State the preparation type.
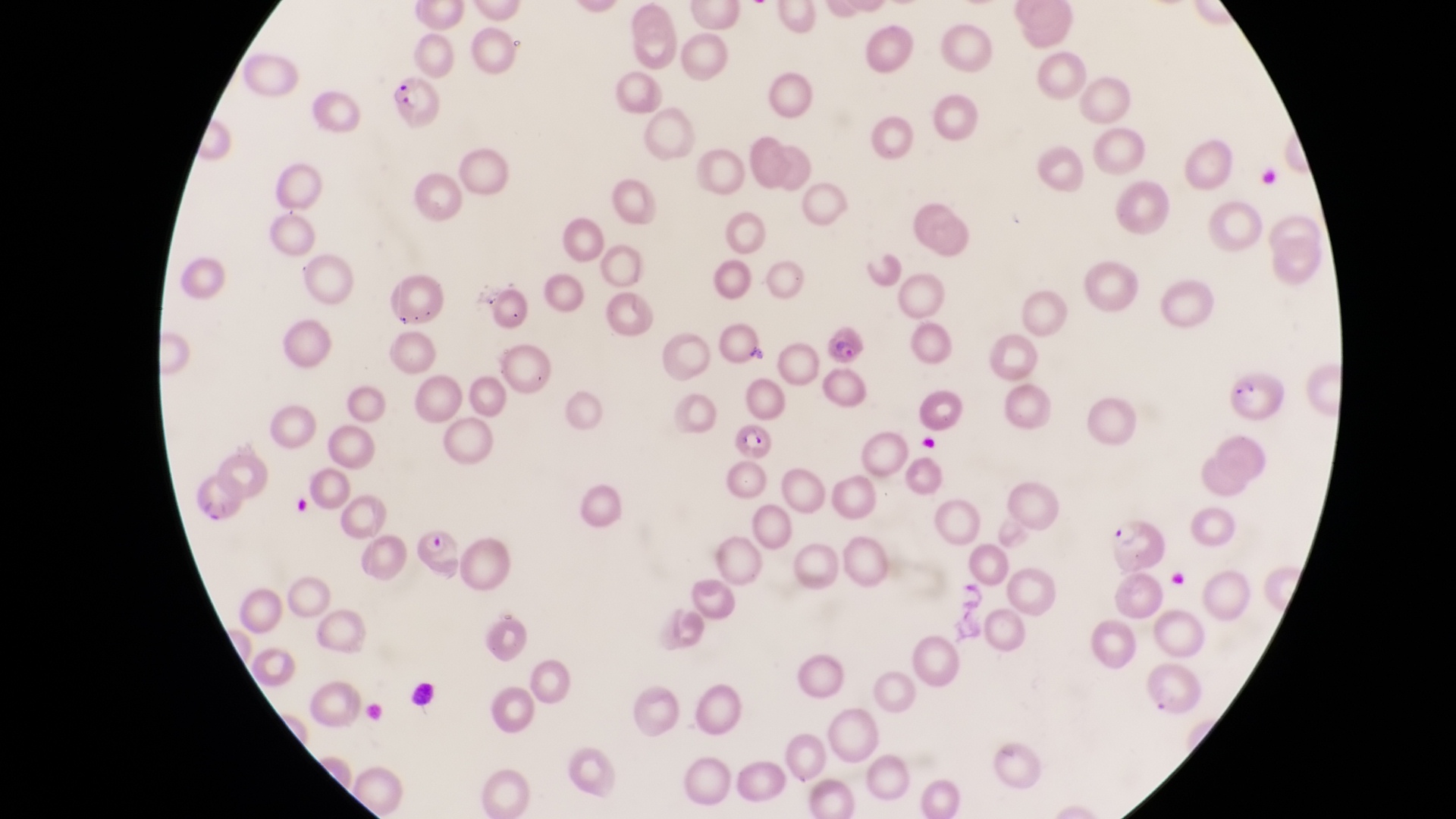
Thin blood smear.

Approximate bounding boxes as left top right bottom in pixels. Leukocyte locations: 409 680 441 712. Parasitised red blood cell locations: 384 74 445 128; 825 327 870 366; 1226 367 1287 428; 727 420 773 465; 191 473 249 529; 410 513 465 582; 1107 516 1168 576. One field of view. Sample from Uganda. Captured by a smartphone held over the eyepiece of an Olympus CX-23 microscope. At a magnification of 1000x. Image is 1456×819 pixels.